Report the malaria status of this cell.
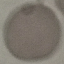

It is uninfected.

Summary:
  - Image type: automatically extracted cell patch, resized to 64 × 64 pixels
  - Capture: smartphone through the microscope eyepiece
  - Stain: Giemsa
  - Preparation: thin blood film